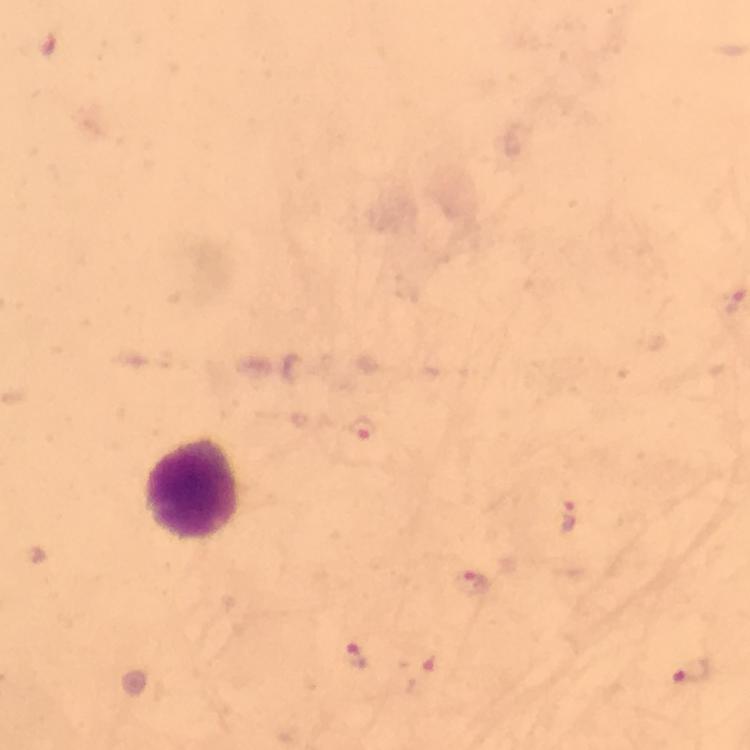 Approximate centers as [x, y] in pixels. Plasmodium parasite locations: [360, 429], [568, 517], [474, 583], [352, 651], [692, 672]. Leukocyte locations: [196, 490]. Immersion oil was used. Thick blood film. Giemsa stain. 100x magnification. From a malaria diagnostic workup. A crop from one field of view. Photographed with a smartphone mounted on the microscope. Image is 750×750 pixels.